Comment on the morphology of the erythrocytes.
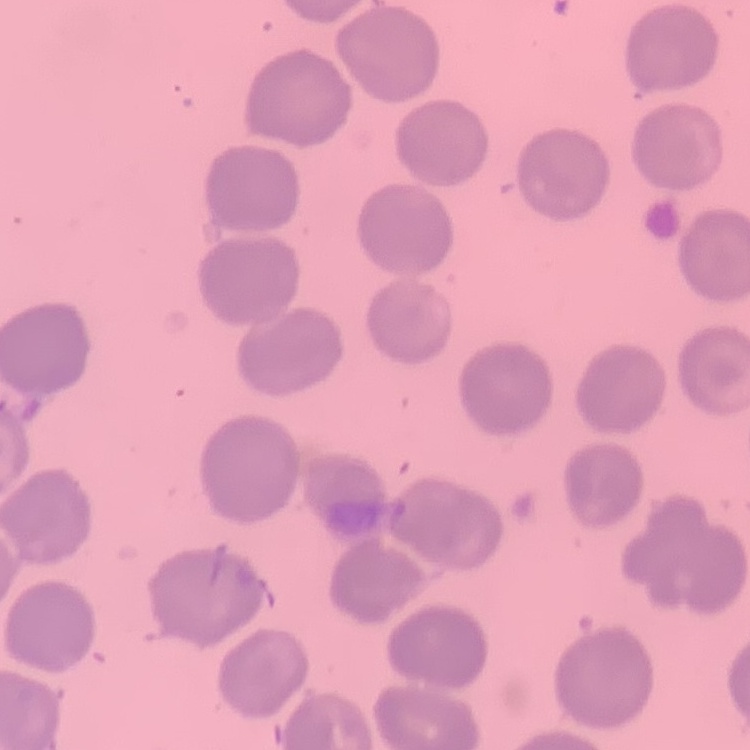

They show no rouleaux formation.

image type = one tile cut from a larger photomicrograph
stain = Field's or Giemsa
preparation = thin peripheral smear